Assess this cell for malaria.
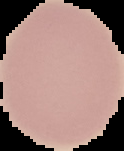

Uninfected.

image size = 124×151 pixels
preparation = thin blood film
image type = cell region segmented out of the field of view; surrounding area masked to black